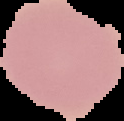 Result: no malaria parasites detected. Segmented cell region on a black background. Image is 124×121 pixels. From a thin blood film.